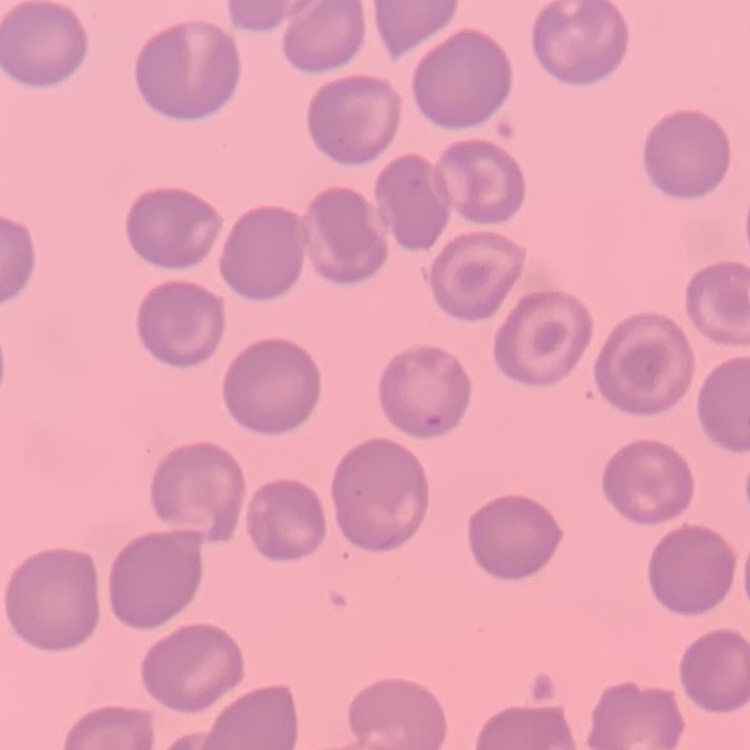

{
  "erythrocyte_morphology": "no rouleaux formation",
  "preparation": "thin blood smear",
  "image_type": "square crop of a larger photomicrograph",
  "stain": "Field's or Giemsa"
}